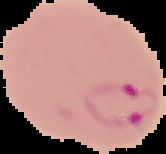

{
  "result": "Plasmodium parasites identified",
  "image_type": "cell region segmented out of the field of view; surrounding area masked to black",
  "image_size": "166×154 pixels",
  "preparation": "thin blood smear"
}